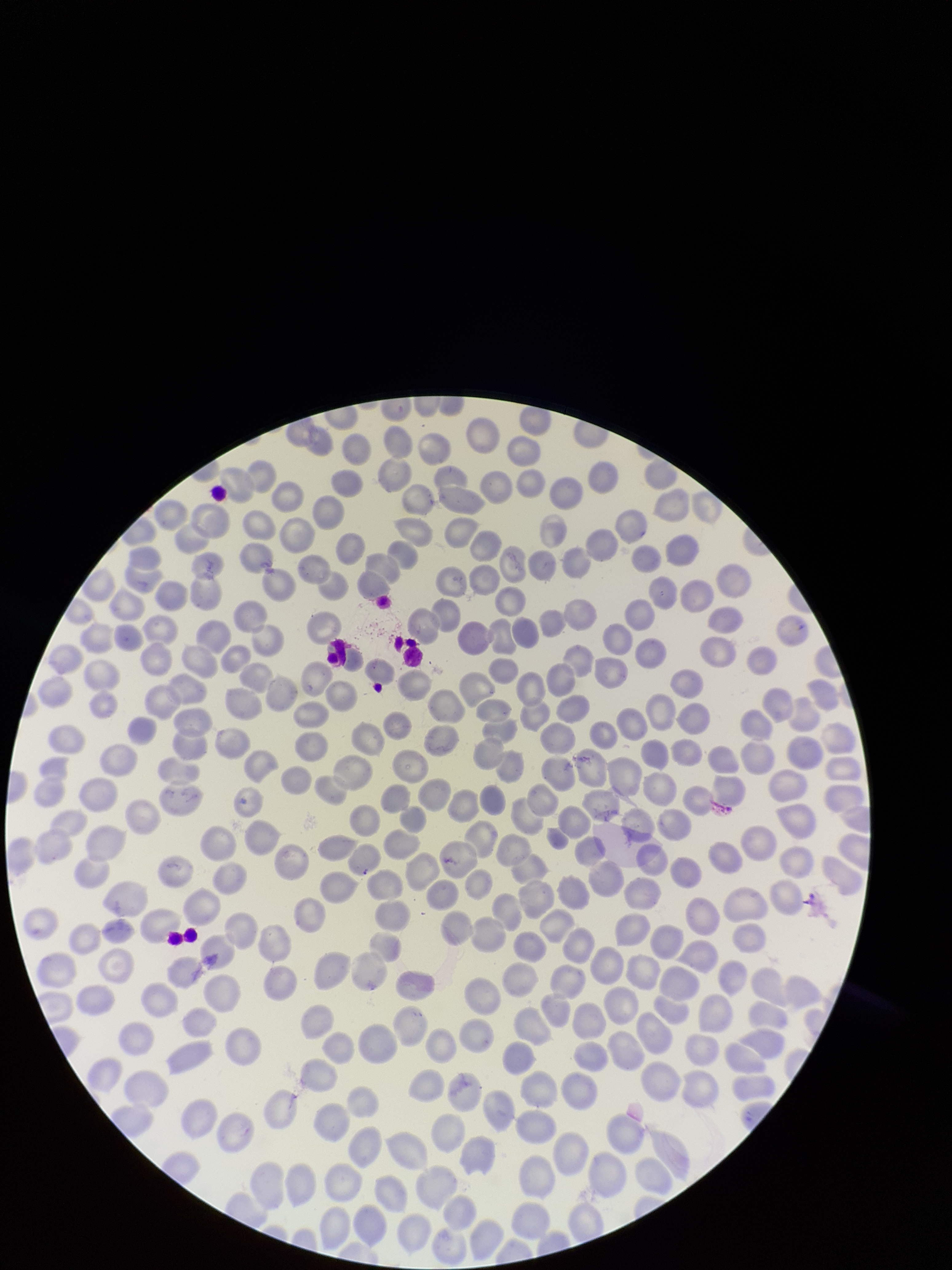

Preparation: thin blood smear. Patient malaria status: infected. Giemsa stain. Single field of view. Smartphone photograph taken through the eyepiece of a microscope. Image is 952×1270 pixels. Red blood cell count: 291. Parasitized red blood cells: none identified. Species reported for this patient: Plasmodium falciparum. Parasitized red blood cell count: 0.